Evaluate for parasitized red blood cells.
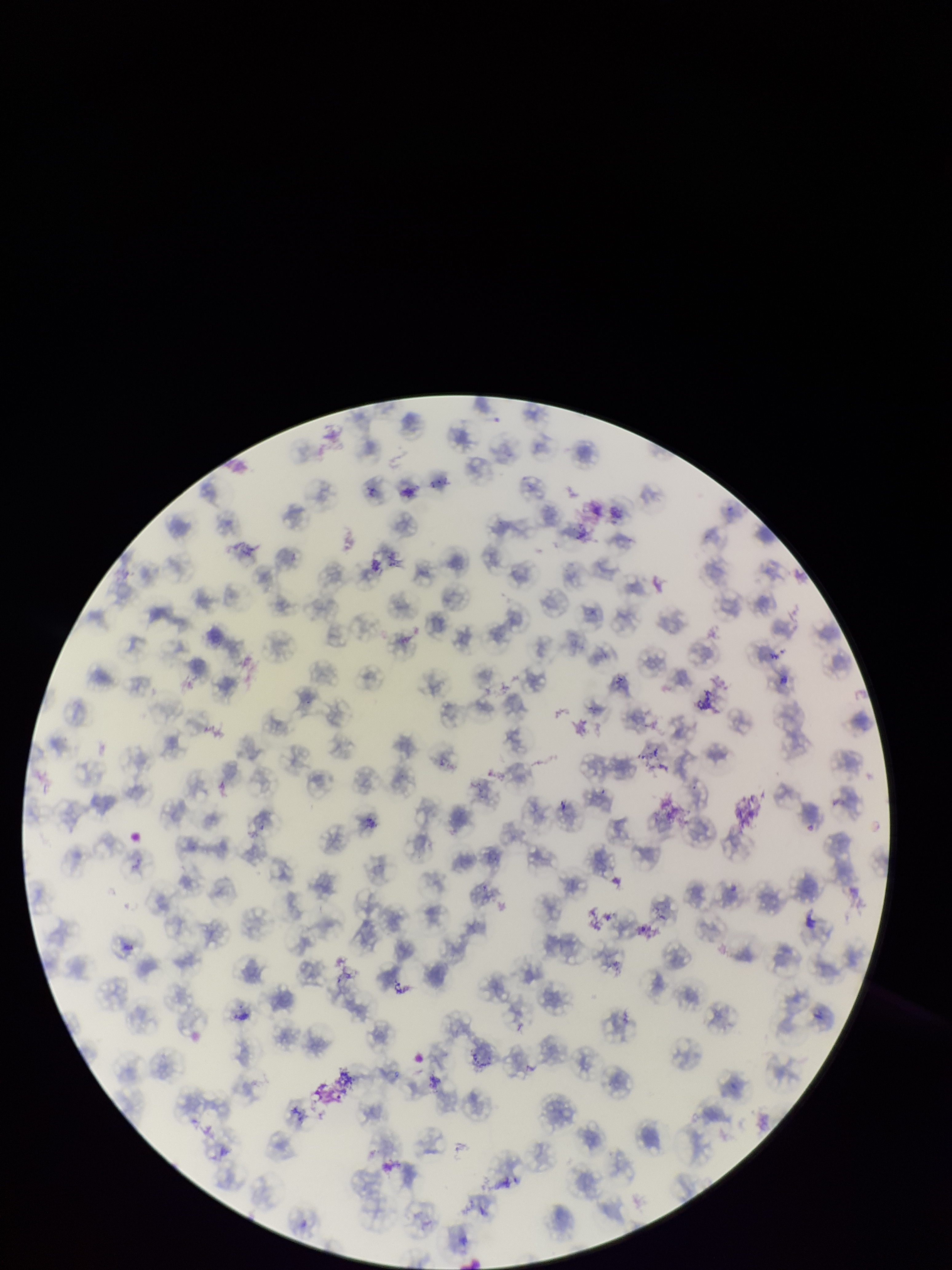

None seen.

image size = 952×1270 pixels
stain = Giemsa
parasitized red blood cell count = 0
species reported for this patient = Plasmodium falciparum
red blood cell count = 118
field of view = one from this slide
patient malaria status = infected
capture = smartphone photograph through the microscope eyepiece
preparation = thin